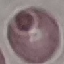 Result: no malaria parasites detected. Acquired by smartphone through the microscope eyepiece. Thin blood smear. Cell patch, automatically extracted from a larger field of view and resized to 64 × 64 pixels. Giemsa-stained preparation.